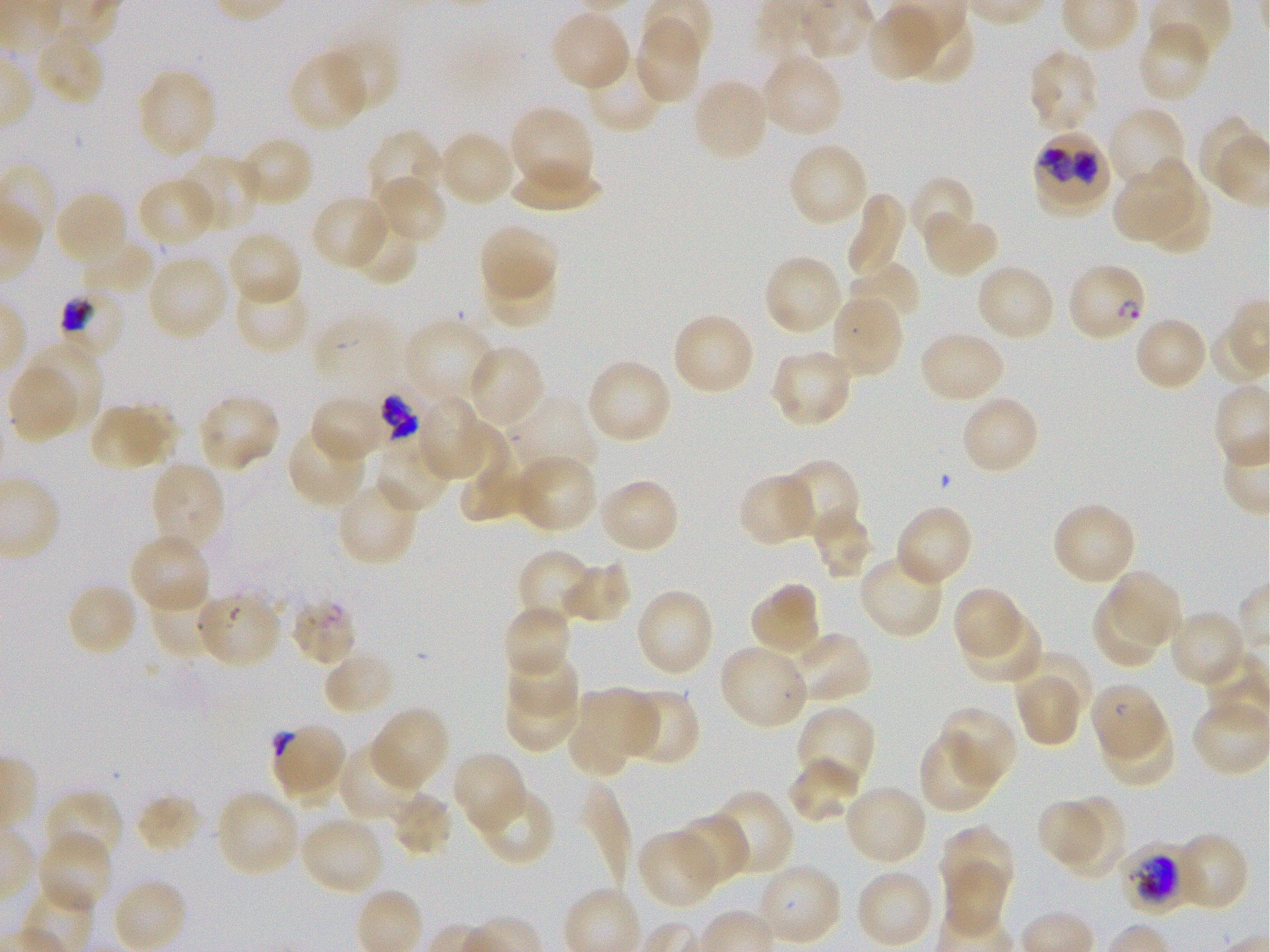

Approximate bounding boxes as {x1, y1, x2, y2} in pixels. Not every red blood cell is marked. A life-cycle stage — or a range of stages, where the recorded stages span more than one — follows each staged infected red blood cell.
Summary:
  - Locations of infected red blood cells: {1030, 127, 1115, 216}; {1066, 261, 1148, 343} ring; {54, 289, 127, 364} trophozoite; {372, 387, 422, 448}; {289, 595, 356, 666}; {1090, 681, 1167, 762}; {1120, 845, 1193, 913} late trophozoite to early schizont
  - Locations of uninfected red blood cells: {867, 4, 951, 82}, {549, 9, 632, 91}, {907, 17, 978, 92}, {634, 18, 705, 106}, {1137, 21, 1211, 105}, {34, 29, 106, 107}, {323, 36, 399, 115}, {586, 48, 667, 133}, {1026, 48, 1100, 136}, {289, 49, 371, 131}, {758, 52, 844, 140}, {135, 68, 218, 160}, {690, 77, 770, 164}, {508, 105, 596, 200}, {1107, 106, 1189, 191}, {367, 129, 445, 211}, {435, 130, 517, 208}, {237, 135, 314, 208}, {787, 143, 870, 228}, {177, 154, 262, 235}, {1115, 158, 1200, 241}, {507, 164, 603, 214}, {373, 174, 448, 245}, {907, 175, 977, 249}, {137, 176, 219, 249}, {1143, 182, 1210, 261}, {53, 190, 130, 268}, {844, 192, 907, 282}, {310, 194, 391, 271}, {347, 208, 418, 285}, {920, 208, 998, 279}, {479, 223, 558, 300}, {226, 230, 302, 307}, {80, 236, 158, 296}, {762, 253, 844, 337}, {146, 254, 230, 342}, {847, 262, 922, 330}, {974, 263, 1056, 343}, {487, 265, 557, 327}, {232, 274, 312, 354}, {829, 292, 904, 378}, {671, 312, 756, 397}, {309, 315, 409, 397}, {1132, 315, 1208, 393}, {404, 317, 499, 410}, {918, 329, 1006, 405}, {466, 344, 545, 430}, {770, 348, 855, 428}, {586, 357, 672, 445}, {6, 361, 81, 443}, {195, 393, 282, 474}, {308, 393, 389, 464}, {960, 393, 1040, 476}, {503, 395, 597, 481}, {417, 396, 493, 483}, {114, 398, 188, 464}, {87, 406, 165, 472}, {459, 421, 522, 522}, {287, 424, 368, 508}, {373, 436, 456, 515}, {514, 459, 597, 528}, {778, 459, 861, 541}, {153, 464, 225, 549}, {738, 471, 819, 546}, {597, 477, 680, 555}, {337, 478, 421, 565}, {1051, 501, 1137, 587}, {894, 504, 973, 588}, {808, 506, 875, 581}, {133, 538, 207, 609}, {517, 549, 596, 626}, {858, 553, 945, 640}, {561, 561, 632, 624}, {1112, 575, 1177, 645}, {65, 582, 139, 658}, {749, 582, 821, 660}, {949, 584, 1024, 663}, {149, 586, 221, 661}, {634, 589, 715, 679}, {1089, 590, 1166, 668}, {196, 595, 279, 665}, {501, 604, 569, 673}, {1167, 609, 1246, 688}, {965, 615, 1042, 684}, {781, 631, 872, 704}, {717, 644, 809, 731}, {322, 649, 394, 716}, {507, 650, 580, 714}, {1011, 653, 1091, 722}, {1014, 670, 1081, 751}, {580, 684, 661, 759}, {633, 688, 700, 761}, {504, 692, 578, 752}, {1191, 697, 1270, 776}, {367, 707, 448, 794}, {793, 707, 876, 796}, {939, 707, 1017, 790}, {1100, 713, 1176, 788}, {568, 723, 629, 776}, {918, 732, 999, 814}, {337, 744, 422, 823}, {452, 751, 528, 833}, {788, 756, 864, 823}, {842, 783, 928, 867}, {473, 784, 555, 866}, {581, 784, 633, 894}, {709, 788, 794, 877}, {44, 789, 123, 868}, {214, 789, 301, 880}, {389, 790, 452, 856}, {1049, 791, 1126, 878}, {135, 794, 201, 854}, {1034, 799, 1108, 866}, {672, 812, 750, 887}, {299, 815, 386, 897}, {940, 824, 1026, 889}, {636, 829, 722, 908}, {36, 831, 113, 913}, {1172, 831, 1249, 912}, {753, 861, 841, 948}, {944, 863, 1009, 935}, {854, 868, 935, 948}, {111, 878, 188, 952}
  - Locations of red blood cells of indeterminate infection status: {270, 722, 348, 804}
  - Life-cycle stages observed: ring, trophozoite
  - Field of view: one from this slide
  - Donor blood group: O+
  - Stain: Giemsa
  - Image size: 1270×952 pixels
  - Objective: 100x, oil immersion, numerical aperture 1.25
  - Culture: static in-vitro Plasmodium falciparum strain 3D7
  - Preparation: thin blood smear